Report the malaria status of this cell.
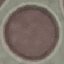
It is uninfected.

capture = smartphone camera at the microscope eyepiece
preparation = thin smear
image type = cell patch, automatically extracted from a larger field of view and resized to 64 × 64 pixels
stain = Giemsa